Assess this cell for malaria.
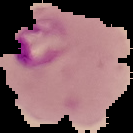
Parasitized.

preparation = thin blood film
image size = 133×133 pixels
image type = segmented cell region on a black background